Classify this cell by malaria status.
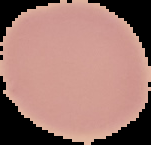

It is uninfected.

From a thin blood film. Image is 151×145 pixels. Cell region segmented out of the field of view; the surrounding area is masked to black.